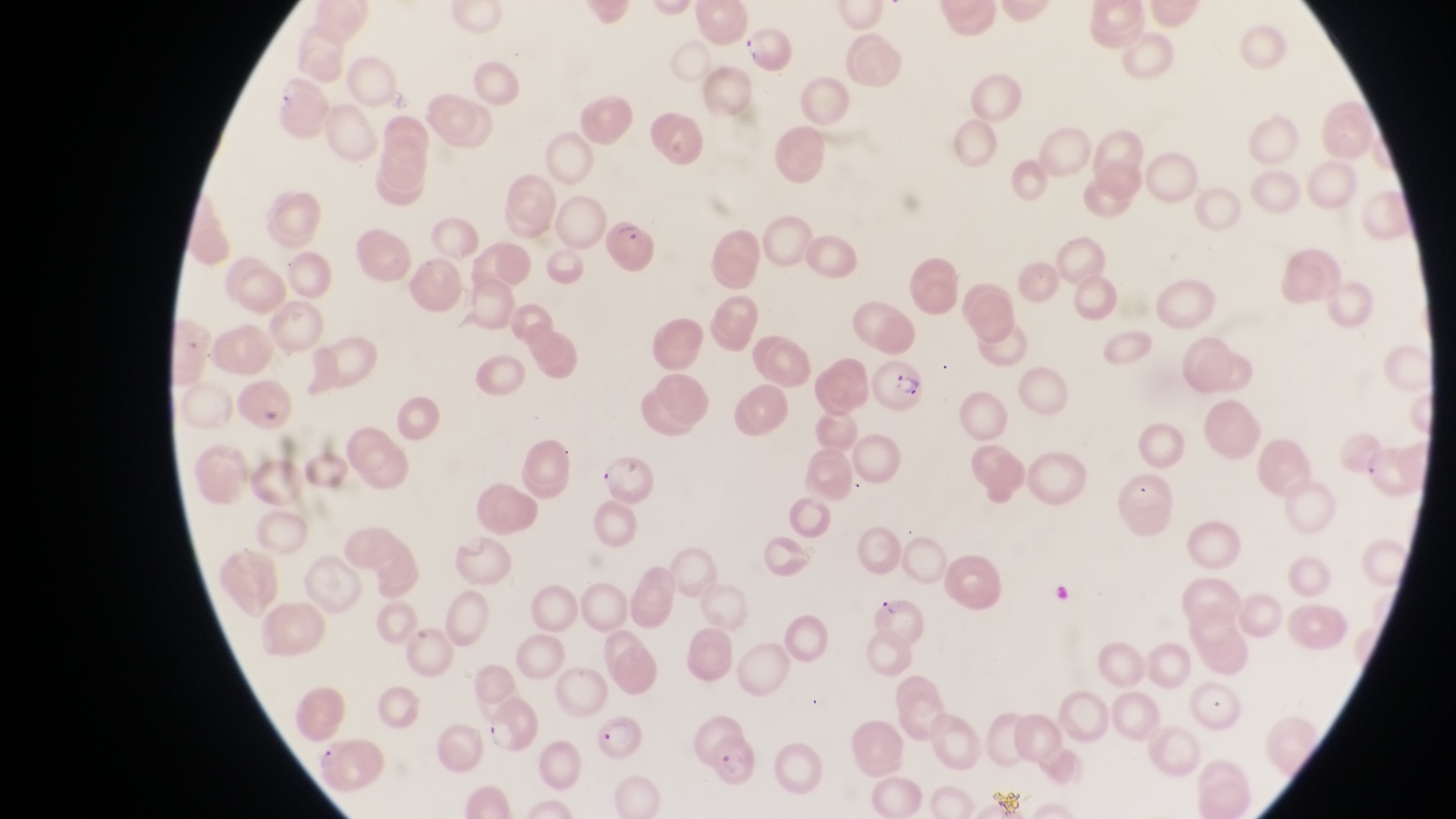
country = Uganda
preparation = thin blood smear
image size = 1456×819 pixels
capture = smartphone photograph through the eyepiece of an Olympus CX-23 microscope
magnification = 1000x
field of view = single
parasitised red blood cell locations = approximate bounding boxes as {left, top, right, bottom} in pixels: {600, 218, 658, 273}, {868, 362, 926, 415}, {482, 700, 538, 753}, {589, 716, 647, 771}